Assess this cell for malaria.
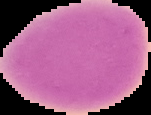

Uninfected.

Image is 151×115 pixels. Cell region segmented out of the field of view; the surrounding area is masked to black. From a thin blood smear.